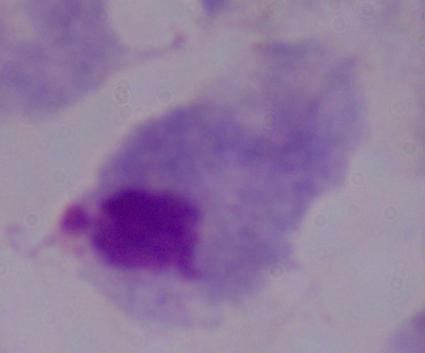

magnification = 1000x
modality = micrograph
identification = trichomonad